Report the malaria status of this cell.
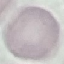

It is uninfected.

preparation = thin blood smear
stain = Giemsa
image type = automatically extracted cell patch, resized to 64 × 64 pixels
capture = smartphone camera at the microscope eyepiece